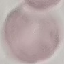
Result: no malaria parasites detected. Thin blood film. Automatically extracted cell patch, resized to 64 × 64 pixels. Photographed with a smartphone camera at the microscope eyepiece. Giemsa stain.